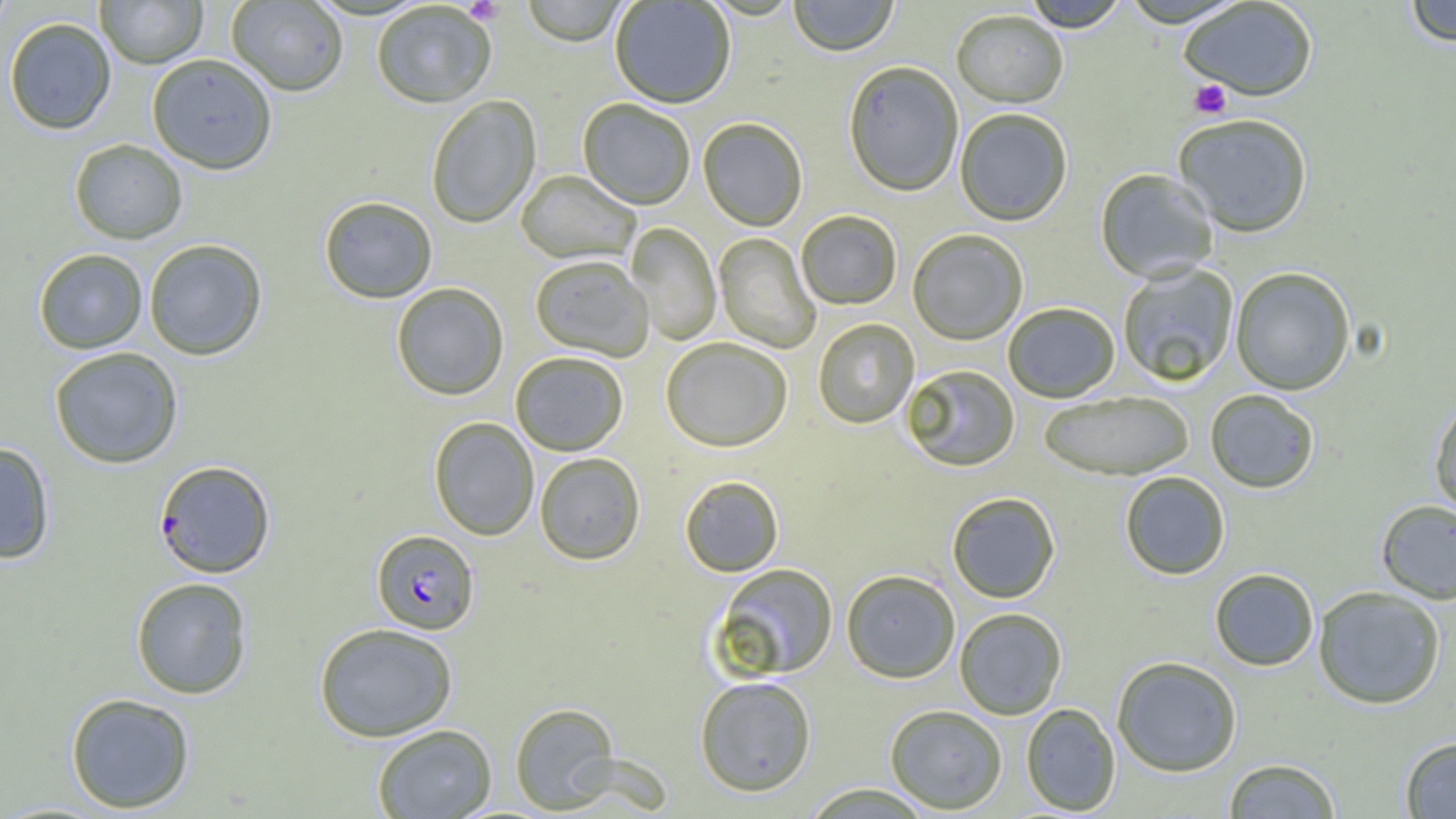
Summary:
  - Coordinate format: approximate bounding boxes as named x1/y1/x2/y2 corners in pixels
  - Plasmodium falciparum-infected red blood cell locations: (x1=154, y1=459, x2=276, y2=579), (x1=371, y1=529, x2=479, y2=635)
  - Uninfected red blood cell locations: (x1=0, y1=0, x2=17, y2=38), (x1=95, y1=0, x2=208, y2=68), (x1=521, y1=0, x2=630, y2=48), (x1=789, y1=0, x2=898, y2=58), (x1=226, y1=1, x2=348, y2=96), (x1=610, y1=1, x2=736, y2=110), (x1=1019, y1=1, x2=1129, y2=34), (x1=1117, y1=1, x2=1251, y2=30), (x1=1179, y1=1, x2=1318, y2=104), (x1=1403, y1=1, x2=1456, y2=48), (x1=371, y1=3, x2=497, y2=109), (x1=951, y1=12, x2=1068, y2=110), (x1=3, y1=17, x2=117, y2=134), (x1=147, y1=54, x2=278, y2=175), (x1=843, y1=63, x2=963, y2=198), (x1=426, y1=96, x2=541, y2=229), (x1=577, y1=99, x2=695, y2=211), (x1=956, y1=110, x2=1073, y2=227), (x1=1173, y1=116, x2=1313, y2=239), (x1=698, y1=119, x2=807, y2=232), (x1=69, y1=139, x2=188, y2=244), (x1=1095, y1=169, x2=1218, y2=283), (x1=516, y1=171, x2=640, y2=266), (x1=319, y1=196, x2=437, y2=304), (x1=796, y1=212, x2=902, y2=311), (x1=626, y1=222, x2=722, y2=345), (x1=908, y1=231, x2=1028, y2=346), (x1=714, y1=233, x2=821, y2=354), (x1=143, y1=239, x2=268, y2=361), (x1=33, y1=248, x2=148, y2=353), (x1=530, y1=256, x2=653, y2=362), (x1=1117, y1=263, x2=1239, y2=387), (x1=1230, y1=268, x2=1355, y2=396), (x1=391, y1=283, x2=509, y2=401), (x1=1004, y1=304, x2=1119, y2=403), (x1=813, y1=319, x2=919, y2=429), (x1=661, y1=339, x2=792, y2=454), (x1=49, y1=347, x2=184, y2=469), (x1=511, y1=352, x2=628, y2=456), (x1=902, y1=365, x2=1019, y2=472), (x1=1205, y1=390, x2=1319, y2=494), (x1=1038, y1=393, x2=1193, y2=482), (x1=1429, y1=395, x2=1456, y2=523), (x1=429, y1=417, x2=539, y2=541), (x1=0, y1=442, x2=55, y2=564), (x1=535, y1=453, x2=645, y2=565), (x1=1120, y1=472, x2=1230, y2=580), (x1=680, y1=476, x2=784, y2=577), (x1=947, y1=493, x2=1060, y2=604), (x1=1376, y1=500, x2=1456, y2=605), (x1=713, y1=564, x2=838, y2=680), (x1=1209, y1=568, x2=1319, y2=671), (x1=841, y1=570, x2=960, y2=684), (x1=131, y1=577, x2=253, y2=699), (x1=1313, y1=587, x2=1446, y2=709), (x1=954, y1=608, x2=1067, y2=720), (x1=314, y1=623, x2=458, y2=742), (x1=1112, y1=657, x2=1243, y2=777), (x1=695, y1=675, x2=816, y2=797), (x1=64, y1=692, x2=195, y2=813), (x1=510, y1=703, x2=619, y2=813), (x1=1021, y1=703, x2=1121, y2=815), (x1=885, y1=705, x2=1007, y2=814), (x1=372, y1=724, x2=497, y2=819), (x1=1399, y1=736, x2=1456, y2=818), (x1=1222, y1=758, x2=1342, y2=818), (x1=799, y1=783, x2=936, y2=818)
  - Platelet locations: (x1=463, y1=0, x2=503, y2=24), (x1=1189, y1=80, x2=1232, y2=120)
  - Slide-level diagnosis: Plasmodium falciparum
  - Image size: 1456×819 pixels
  - Field of view: single
  - Preparation: thin blood smear
  - Modality: light microscopy
  - Magnification: 1000x